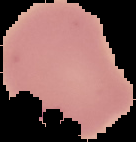

preparation = thin blood smear
image size = 136×142 pixels
malaria status = parasitized
image type = segmented cell region on a black background